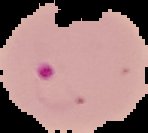

Summary:
  - Preparation: thin blood smear
  - Image size: 148×133 pixels
  - Malaria status: parasitized
  - Image type: cell region segmented out of the field of view; surrounding area masked to black